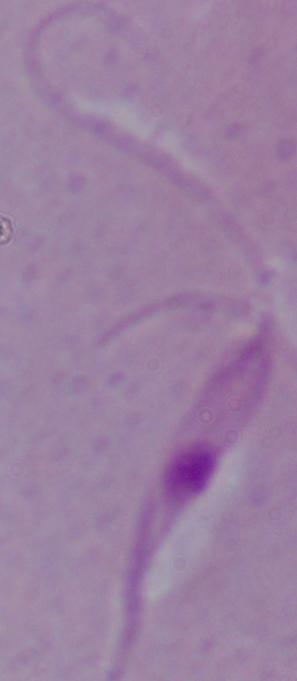

Summary:
  - Identification: Leishmania
  - Magnification: 1000x
  - Modality: micrograph